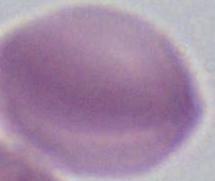
A red blood cell is seen. Photomicrograph. Captured at 1000x magnification.